Report the malaria status of this cell.
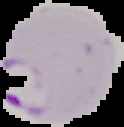
Parasitized.

{
  "image_size": "124×127 pixels",
  "preparation": "thin blood smear",
  "image_type": "cell region segmented out of the field of view; surrounding area masked to black"
}